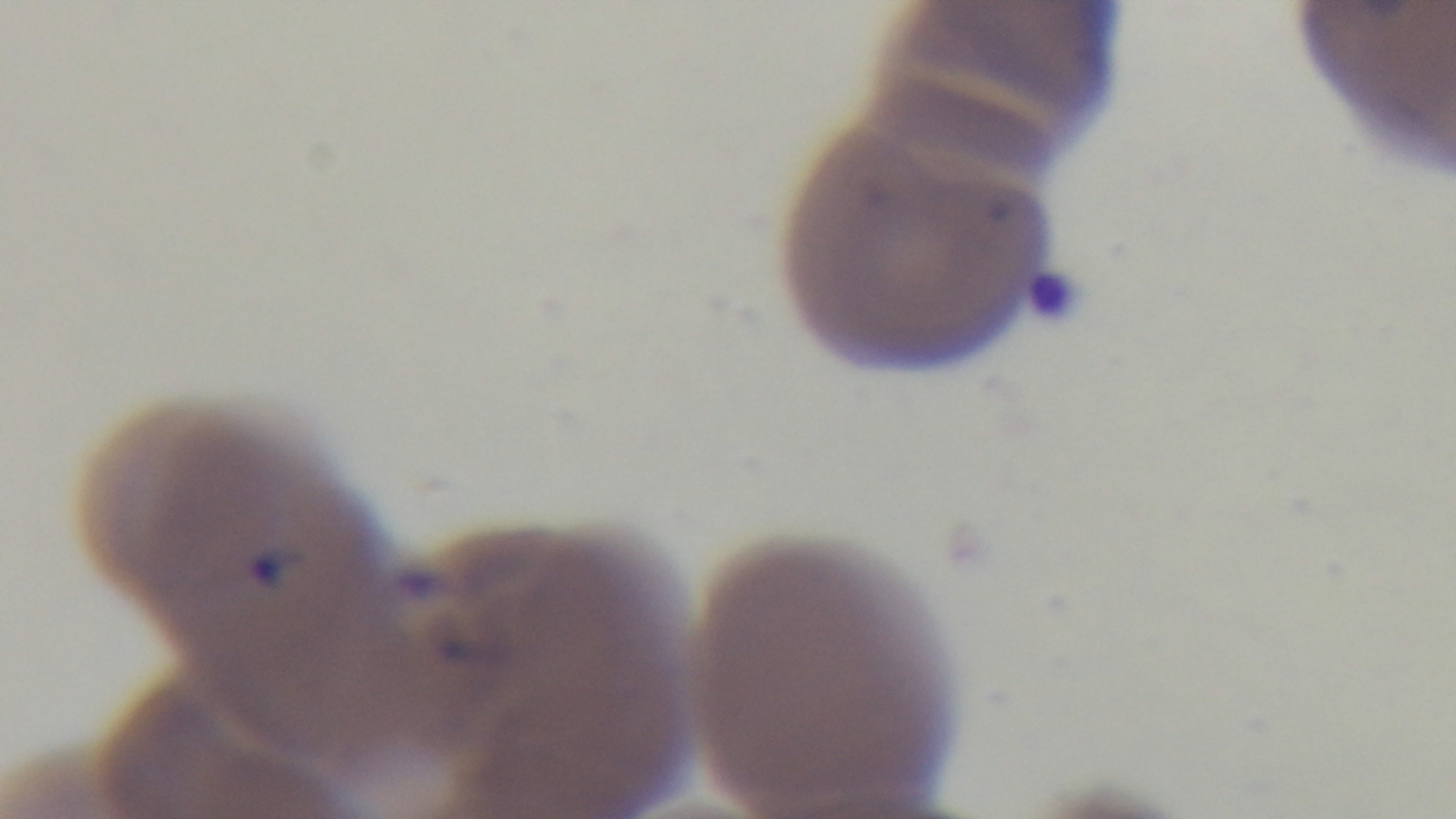
Summary:
  - Capture: mounted 4K digital camera
  - Stain: Giemsa
  - Malaria status: positive
  - Objective: 100x oil immersion
  - Field of view: single
  - Preparation: thin smear
  - Modality: light microscopy